Identify the blood parasite species.
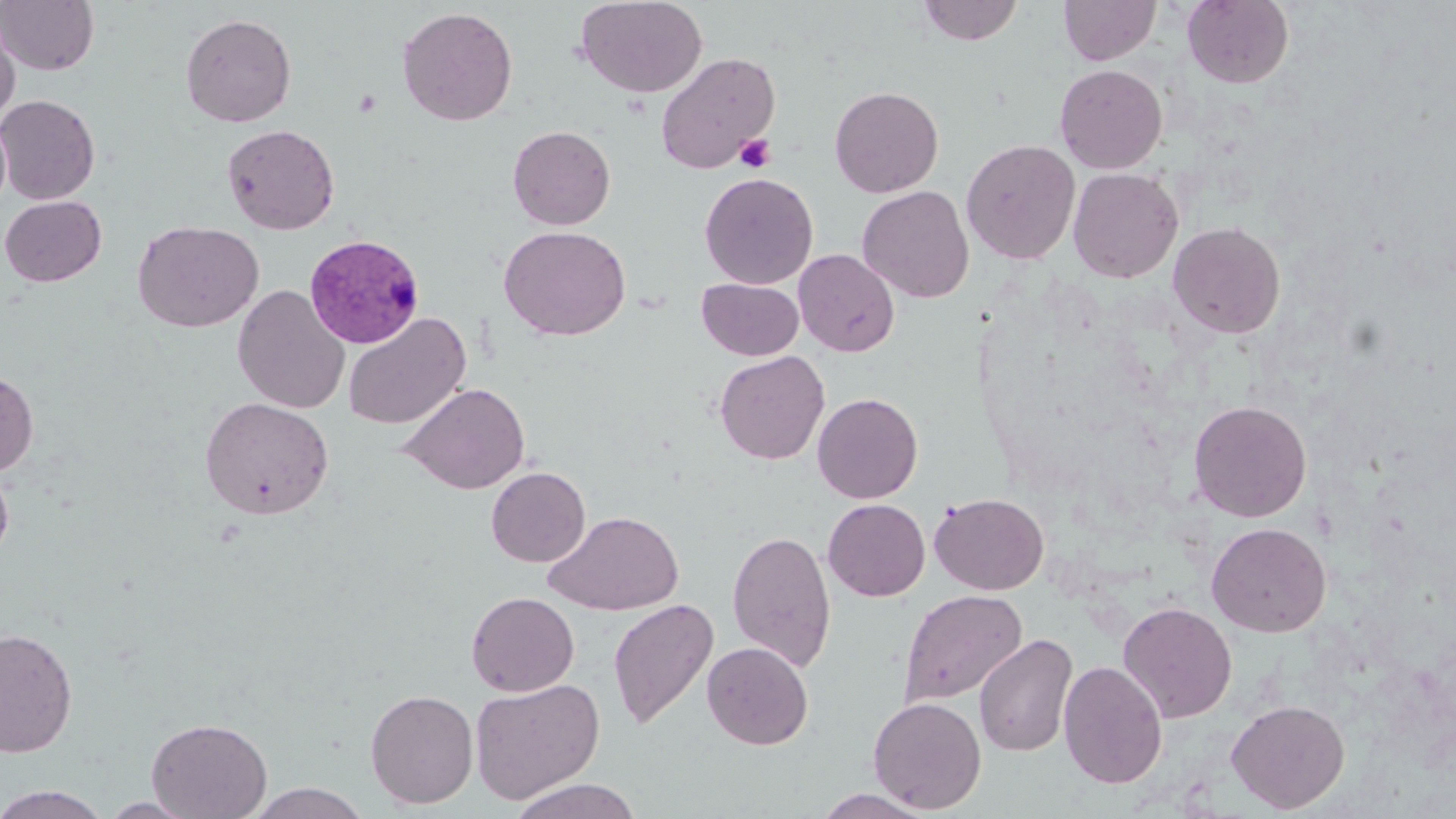

Plasmodium vivax.

Summary:
  - Coordinate format: approximate bounding boxes as [x1, y1, x2, y2] in pixels
  - Platelet locations: [735, 134, 776, 172]
  - Uninfected red blood cell locations: [0, 0, 99, 75], [574, 0, 707, 98], [917, 0, 1023, 45], [1059, 0, 1161, 65], [1182, 0, 1294, 88], [397, 6, 518, 126], [180, 13, 297, 127], [0, 14, 20, 127], [655, 52, 780, 175], [1054, 64, 1168, 173], [829, 86, 944, 197], [0, 95, 100, 204], [0, 113, 11, 216], [222, 124, 340, 235], [508, 125, 615, 230], [961, 139, 1081, 264], [1068, 167, 1183, 283], [700, 172, 818, 289], [857, 185, 974, 302], [0, 195, 106, 286], [133, 220, 264, 332], [1168, 221, 1286, 339], [498, 225, 631, 341], [794, 249, 900, 356], [697, 278, 803, 360], [232, 284, 350, 414], [343, 312, 471, 430], [714, 350, 830, 465], [0, 369, 38, 477], [401, 382, 530, 494], [813, 392, 923, 503], [200, 397, 334, 520], [1188, 400, 1312, 522], [0, 461, 15, 566], [486, 467, 590, 567], [929, 492, 1049, 594], [823, 499, 930, 601], [545, 510, 684, 615], [1206, 522, 1332, 636], [727, 530, 837, 673], [898, 589, 1028, 706], [466, 591, 579, 696], [607, 599, 718, 729], [1118, 601, 1238, 723], [0, 627, 78, 758], [973, 633, 1078, 757], [702, 642, 813, 749], [1058, 660, 1168, 789], [469, 678, 605, 804], [365, 688, 479, 809], [867, 696, 987, 814], [1226, 699, 1350, 813], [146, 717, 272, 818], [507, 779, 644, 819], [245, 783, 372, 819], [0, 785, 110, 819], [810, 789, 938, 818], [99, 797, 201, 818]
  - Plasmodium vivax-infected red blood cell locations: [304, 234, 426, 349]
  - Field of view: one of a larger specimen
  - Magnification: 1000x
  - Modality: light microscopy
  - Image size: 1456×819 pixels
  - Preparation: thin blood smear
  - Stain: May-Grünwald-Giemsa